Report the malaria status of this cell.
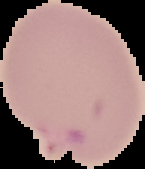
It is parasitized.

From a thin blood smear. The area outside the segmented cell region is set to black. Image is 145×169 pixels.